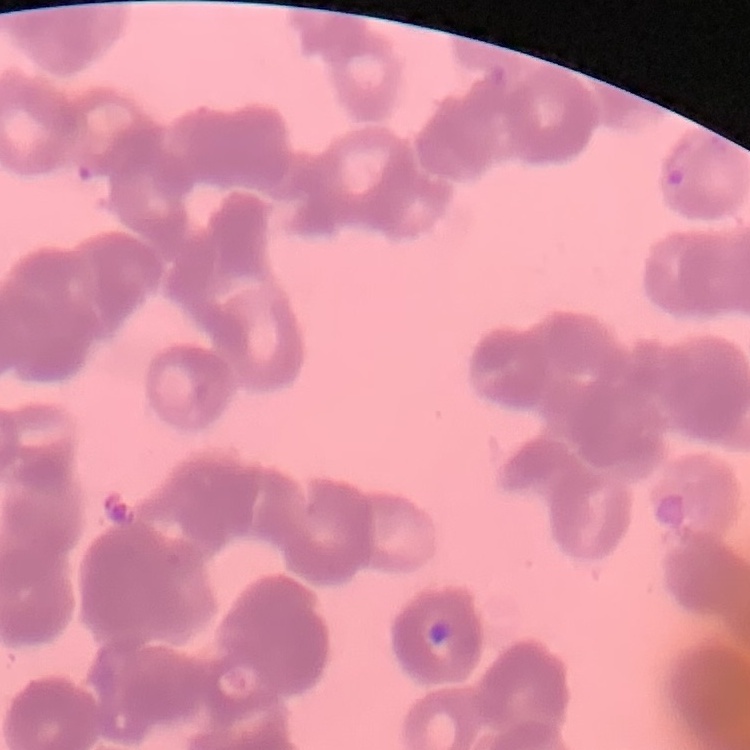

Summary:
  - Erythrocyte morphology: rouleaux formation
  - Image type: one tile cut from a larger photomicrograph
  - Stain: Field's or Giemsa
  - Preparation: thin peripheral smear